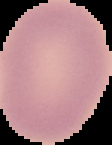

Summary:
  - Image type: segmented cell region on a black background
  - Image size: 112×145 pixels
  - Preparation: thin blood film
  - Result: no malaria parasites seen